Identify the blood parasite species.
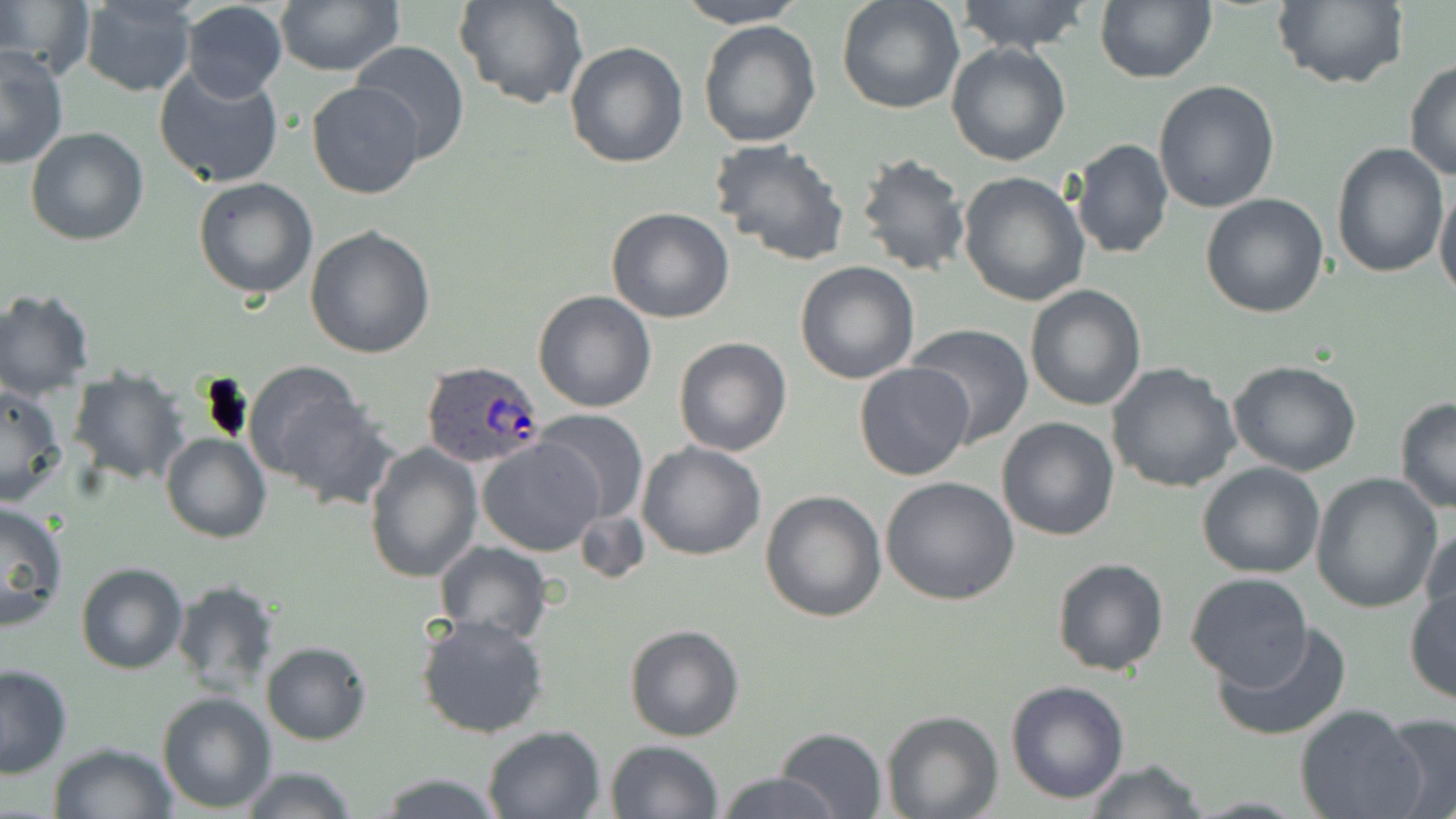
Plasmodium ovale.

Approximate bounding boxes as [x1, y1, x2, y2] in pixels. Plasmodium ovale-infected red blood cell locations: [419, 360, 544, 472]. Uninfected red blood cell locations: [274, 0, 403, 76], [458, 0, 587, 110], [673, 0, 807, 28], [836, 0, 965, 115], [953, 0, 1095, 54], [1095, 0, 1217, 84], [1271, 0, 1406, 90], [0, 1, 90, 78], [77, 1, 197, 96], [179, 2, 288, 103], [697, 20, 822, 149], [348, 40, 472, 166], [564, 42, 689, 169], [946, 43, 1073, 166], [0, 47, 69, 169], [1404, 60, 1456, 183], [153, 62, 286, 189], [306, 80, 425, 200], [1152, 80, 1281, 214], [26, 126, 149, 246], [710, 137, 851, 266], [1070, 139, 1173, 259], [1331, 144, 1449, 278], [856, 151, 973, 278], [958, 171, 1091, 306], [193, 177, 318, 299], [1434, 185, 1456, 302], [1199, 193, 1330, 318], [606, 207, 735, 325], [305, 225, 437, 360], [795, 260, 922, 384], [1025, 285, 1147, 411], [0, 287, 95, 400], [533, 290, 656, 412], [906, 323, 1033, 445], [673, 337, 791, 456], [1228, 361, 1362, 477], [854, 362, 975, 482], [1108, 362, 1240, 493], [243, 365, 372, 497], [68, 366, 189, 486], [0, 384, 67, 506], [1393, 396, 1456, 512], [534, 410, 650, 524], [997, 416, 1120, 540], [161, 432, 270, 542], [478, 438, 602, 555], [364, 439, 483, 583], [637, 441, 766, 561], [1196, 462, 1325, 580], [1310, 474, 1443, 613], [880, 476, 1021, 607], [760, 490, 887, 623], [0, 500, 70, 631], [574, 507, 649, 585], [1420, 523, 1455, 636], [434, 540, 554, 642], [1051, 557, 1170, 676], [76, 563, 188, 675], [1184, 572, 1313, 689], [171, 578, 280, 698], [1404, 585, 1455, 706], [415, 613, 551, 740], [1214, 620, 1353, 740], [624, 623, 745, 742], [261, 641, 372, 746], [0, 664, 73, 778], [1006, 680, 1130, 805], [157, 692, 276, 813], [1296, 706, 1426, 819], [880, 710, 1003, 819], [1378, 713, 1456, 819], [479, 725, 605, 818], [773, 727, 888, 818], [605, 739, 725, 819], [47, 740, 178, 819], [1082, 759, 1208, 819], [237, 766, 362, 819], [372, 772, 509, 818], [714, 772, 845, 818]. Thin blood film. Image is 1456×819 pixels. One field of a larger specimen. 1000x magnification. May-Grünwald-Giemsa-stained preparation. Optical microscopy.